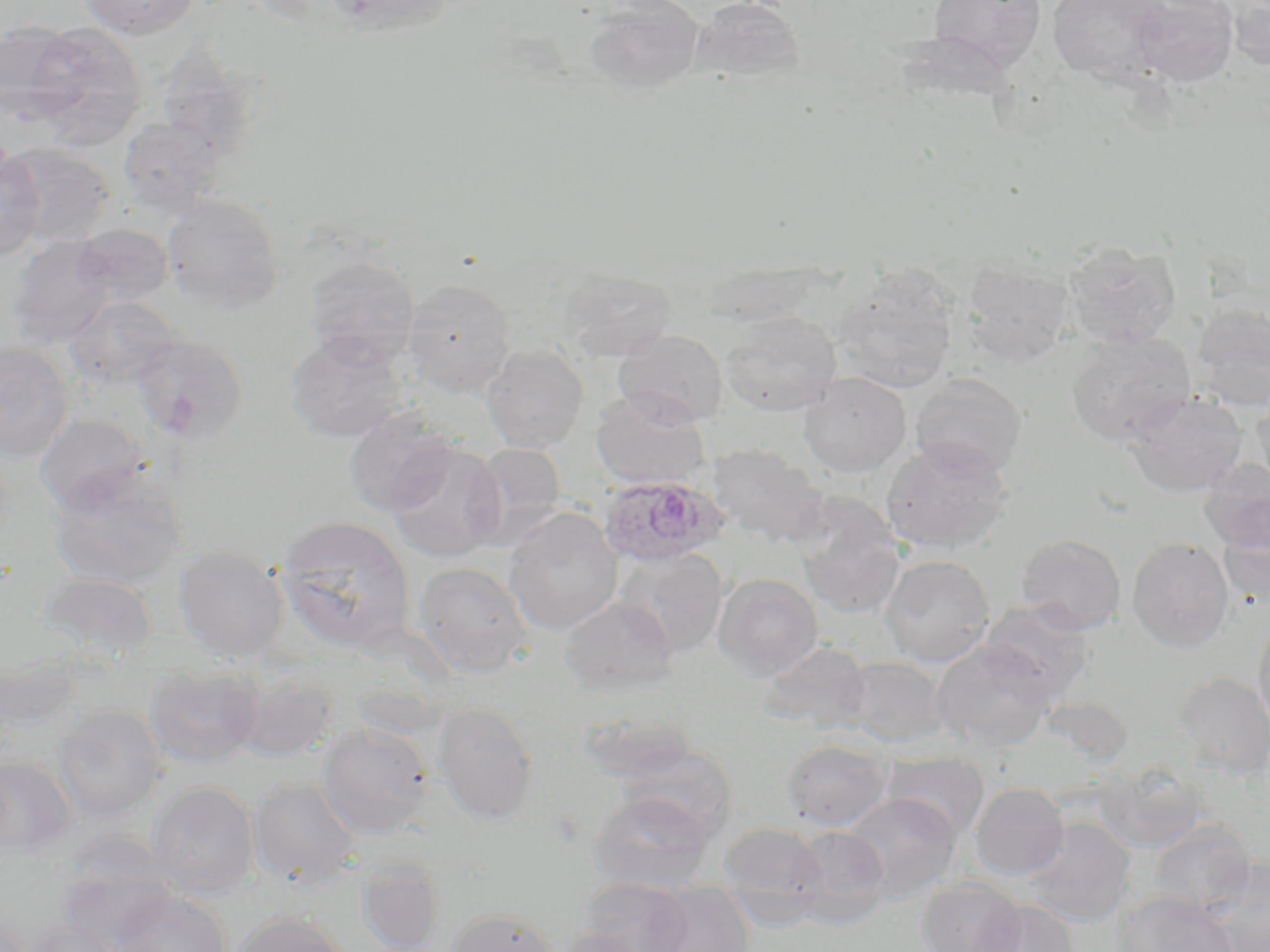
Approximate bounding boxes as (x1, y1, x2, y2) in pixels. Uninfected red blood cell locations: (80, 0, 202, 39), (323, 0, 457, 39), (585, 0, 705, 95), (691, 0, 805, 83), (927, 0, 1047, 76), (1047, 0, 1167, 83), (1132, 0, 1239, 86), (1222, 0, 1270, 70), (0, 20, 82, 123), (23, 21, 147, 148), (156, 39, 264, 164), (118, 117, 225, 219), (2, 142, 115, 248), (0, 149, 46, 261), (162, 193, 284, 313), (74, 224, 173, 306), (7, 236, 117, 349), (1063, 241, 1181, 349), (304, 255, 420, 368), (960, 258, 1076, 364), (557, 267, 676, 362), (695, 267, 823, 327), (831, 272, 959, 392), (403, 279, 516, 396), (64, 295, 180, 390), (1191, 303, 1270, 408), (720, 312, 841, 416), (613, 329, 728, 427), (285, 332, 408, 443), (1067, 332, 1196, 446), (131, 333, 248, 442), (0, 342, 73, 462), (481, 344, 588, 453), (798, 372, 911, 477), (909, 373, 1027, 479), (1250, 388, 1270, 489), (590, 390, 712, 491), (1125, 391, 1247, 497), (344, 409, 457, 515), (35, 413, 148, 514), (881, 439, 1013, 552), (385, 441, 506, 562), (466, 442, 567, 546), (706, 443, 829, 547), (1199, 459, 1270, 554), (48, 474, 185, 590), (792, 501, 905, 619), (504, 507, 623, 636), (276, 516, 416, 654), (1218, 525, 1270, 608), (1016, 534, 1126, 635), (1127, 537, 1234, 653), (174, 546, 289, 660), (614, 546, 729, 657), (879, 554, 995, 667), (413, 561, 533, 677), (35, 572, 159, 661), (713, 573, 823, 680), (559, 597, 678, 695), (979, 599, 1094, 701), (1253, 617, 1270, 739), (758, 640, 872, 731), (932, 640, 1055, 750), (1, 652, 82, 740), (842, 657, 950, 747), (145, 663, 263, 769), (1171, 672, 1270, 778), (231, 673, 340, 762), (1042, 696, 1134, 766), (433, 702, 539, 824), (53, 704, 167, 822), (575, 708, 697, 783), (317, 722, 434, 838), (780, 738, 893, 830), (615, 744, 738, 842), (884, 752, 990, 843), (0, 756, 78, 859), (1098, 762, 1209, 852), (248, 777, 362, 889), (147, 781, 260, 898), (970, 782, 1069, 879), (589, 791, 715, 894), (841, 792, 961, 902), (1023, 817, 1137, 927), (1148, 818, 1255, 917), (718, 821, 828, 918), (787, 825, 891, 927), (53, 844, 178, 952), (356, 855, 445, 952), (1204, 858, 1270, 952), (917, 876, 1026, 952), (577, 877, 694, 952), (648, 884, 754, 952), (111, 889, 231, 952), (1112, 891, 1240, 952), (975, 900, 1078, 952), (444, 907, 559, 952), (232, 911, 352, 952), (1, 913, 33, 952), (23, 916, 125, 952), (553, 928, 652, 952). Plasmodium ovale-infected red blood cell locations: (599, 476, 728, 567). Slide-level diagnosis: Plasmodium ovale. Image is 1270×952 pixels. Thin blood smear. Captured at 1000x magnification. May-Grünwald-Giemsa-stained preparation. Light microscopy. One field of a larger specimen.